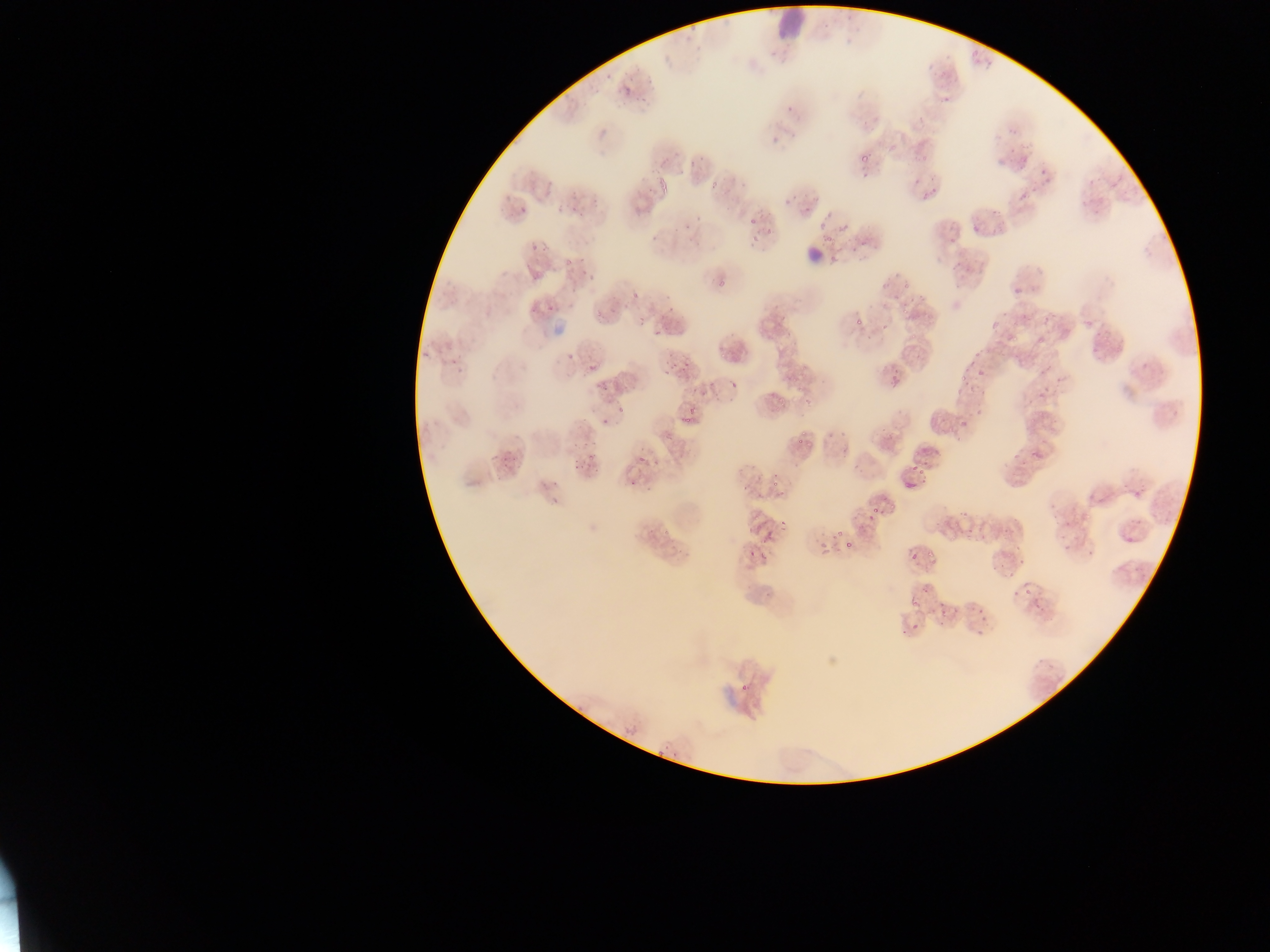

Approximate bounding boxes as {left, top, right, bottom} in pixels.
Summary:
  - Plasmodium parasite locations: {689, 19, 699, 31}, {683, 34, 693, 42}, {603, 73, 614, 80}, {621, 85, 634, 98}, {939, 92, 956, 108}, {644, 95, 648, 103}, {785, 106, 793, 112}, {1006, 124, 1013, 134}, {1007, 147, 1021, 155}, {697, 153, 707, 163}, {859, 156, 868, 163}, {1018, 156, 1029, 168}, {688, 157, 696, 167}, {1038, 170, 1049, 176}, {861, 172, 872, 178}, {910, 178, 920, 185}, {1043, 178, 1051, 184}, {711, 182, 719, 190}, {1025, 189, 1037, 197}, {1018, 192, 1030, 201}, {782, 193, 793, 205}, {920, 195, 928, 203}, {572, 200, 577, 212}, {804, 206, 810, 214}, {990, 206, 998, 214}, {519, 207, 527, 213}, {749, 217, 757, 224}, {840, 220, 850, 231}, {683, 221, 691, 230}, {817, 225, 825, 231}, {766, 226, 774, 235}, {752, 233, 761, 241}, {652, 234, 658, 242}, {823, 235, 833, 243}, {949, 236, 957, 245}, {531, 243, 540, 251}, {562, 258, 572, 269}, {578, 269, 587, 274}, {718, 275, 729, 289}, {588, 276, 597, 282}, {881, 280, 892, 290}, {902, 282, 909, 291}, {1013, 288, 1027, 295}, {633, 291, 641, 300}, {665, 296, 673, 301}, {547, 301, 557, 312}, {623, 302, 629, 310}, {1001, 309, 1009, 316}, {1042, 314, 1051, 321}, {637, 315, 646, 325}, {856, 319, 864, 327}, {989, 321, 999, 329}, {880, 323, 889, 330}, {653, 329, 663, 336}, {1010, 334, 1024, 345}, {719, 348, 728, 359}, {567, 349, 578, 361}, {973, 351, 982, 360}, {683, 357, 690, 372}, {671, 359, 677, 370}, {589, 362, 600, 370}, {962, 365, 970, 373}, {978, 370, 985, 379}, {1038, 370, 1047, 377}, {663, 371, 671, 375}, {898, 373, 903, 384}, {959, 374, 967, 380}, {791, 375, 799, 383}, {888, 376, 896, 384}, {593, 382, 602, 389}, {700, 390, 708, 396}, {803, 394, 816, 405}, {777, 395, 785, 404}, {688, 402, 696, 415}, {683, 415, 691, 423}, {601, 417, 610, 425}, {960, 420, 970, 428}, {800, 431, 809, 438}, {593, 438, 598, 446}, {839, 447, 847, 454}, {494, 451, 502, 459}, {1012, 451, 1021, 459}, {1032, 451, 1043, 456}, {638, 453, 644, 463}, {573, 458, 581, 464}, {651, 458, 660, 464}, {503, 460, 511, 470}, {910, 463, 919, 472}, {587, 465, 595, 471}, {918, 468, 925, 476}, {771, 474, 779, 481}, {551, 479, 560, 487}, {741, 481, 751, 492}, {773, 481, 782, 487}, {551, 499, 559, 505}, {958, 511, 966, 516}, {867, 515, 873, 523}, {1052, 515, 1060, 521}, {781, 521, 789, 527}, {746, 525, 754, 533}, {836, 529, 842, 537}, {966, 531, 976, 535}, {759, 535, 769, 543}, {844, 537, 853, 548}, {747, 550, 757, 557}, {761, 550, 768, 561}, {910, 551, 916, 561}, {1017, 556, 1026, 563}, {1008, 572, 1017, 578}, {1024, 589, 1033, 597}, {911, 598, 917, 607}, {939, 600, 945, 609}, {1033, 603, 1042, 610}, {938, 607, 947, 618}, {975, 608, 985, 615}, {912, 625, 920, 632}, {976, 626, 984, 634} | approximate {x, y} pixel centers of objects too small to bound: {773, 141}, {648, 189}, {934, 193}, {582, 215}, {828, 215}, {698, 218}, {974, 231}, {862, 242}, {670, 308}, {531, 310}, {905, 312}, {912, 336}, {1041, 342}, {453, 363}, {972, 363}, {734, 385}, {693, 390}, {620, 410}, {800, 442}, {586, 444}, {574, 445}, {591, 457}, {575, 468}, {633, 484}, {543, 485}, {783, 495}, {885, 499}, {875, 510}, {666, 530}, {1067, 547}, {929, 554}, {1003, 564}, {995, 567}, {927, 591}, {1015, 593}, {904, 632}
  - Leukocyte locations: {771, 1, 806, 40}, {802, 247, 822, 263}
  - Field of view: single
  - Image size: 1270×952 pixels
  - Preparation: thin blood film
  - Capture: mobile-phone photograph through a microscope
  - Country: Ghana